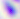

identification: Toxoplasma gondii
modality: photomicrograph
magnification: 400x